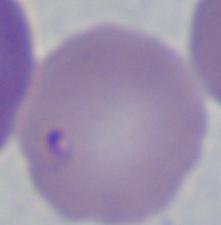

{
  "identification": "Babesia",
  "modality": "micrograph",
  "magnification": "1000x"
}